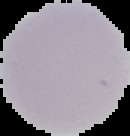

result: no malaria parasites seen
image_size: 130×136 pixels
preparation: thin blood smear
image_type: segmented cell region on a black background